Report the malaria status of this cell.
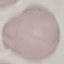
Uninfected.

preparation = thin blood smear
stain = Giemsa
capture = smartphone camera at the microscope eyepiece
image type = cell patch, automatically extracted from a larger field of view and resized to 64 × 64 pixels